State the preparation type.
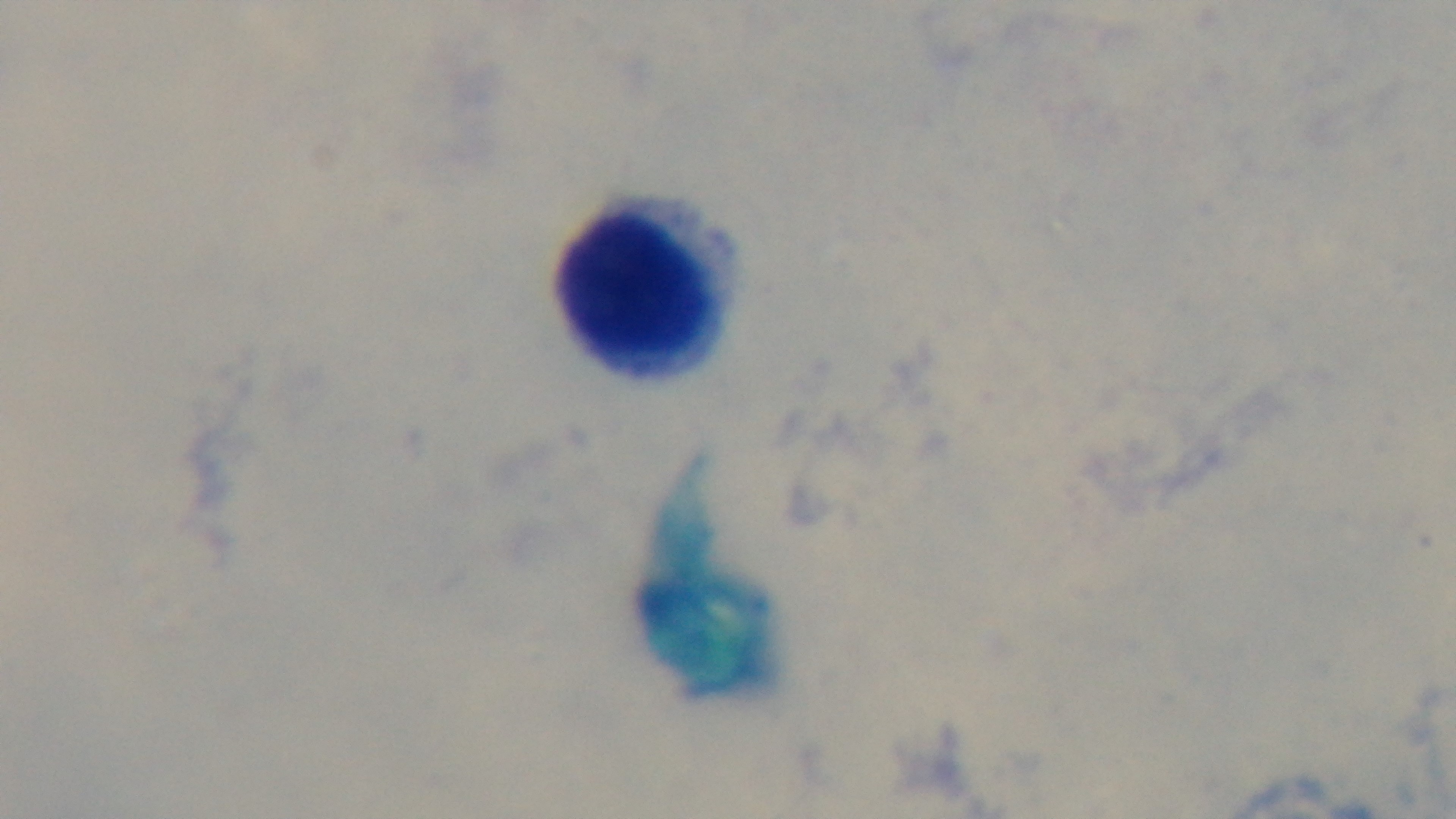
It is a thick blood film.

field of view = one from the slide
stain = Giemsa
modality = light microscopy
objective = 100x oil immersion
capture = mounted 4K digital camera
malaria status = negative